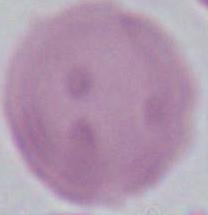

magnification: 1000x
modality: photomicrograph
identification: red blood cell